State which cell type is depicted.
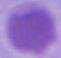

An erythrocyte.

{
  "modality": "photomicrograph",
  "magnification": "1000x"
}